Locate every Plasmodium vivax-infected red blood cell.
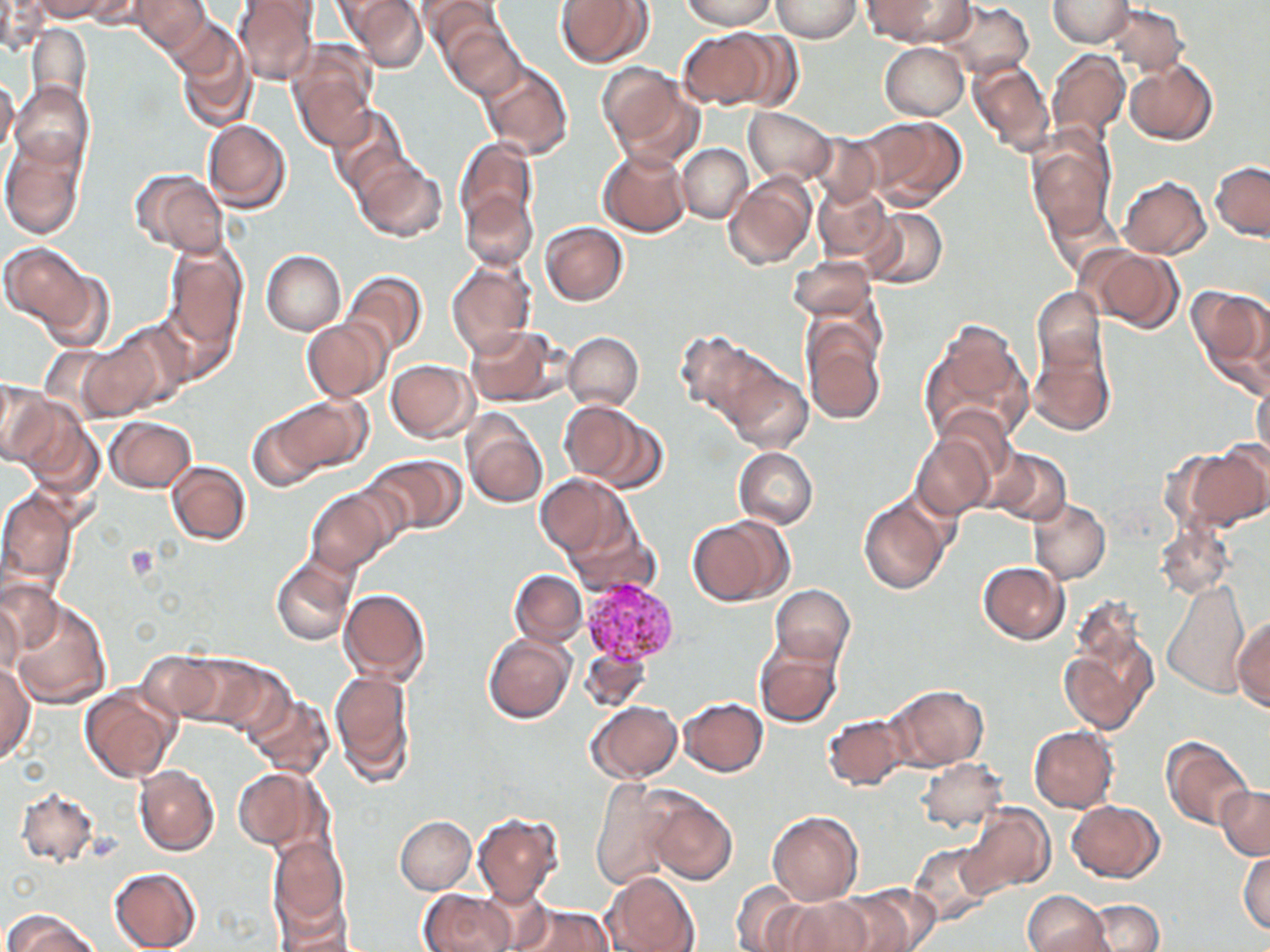

Approximate bounding boxes as (x1,y1)-(x2,y2) corner pairs in pixels.
Plasmodium vivax-infected red blood cells: (581,579)-(678,664).

slide-level diagnosis = Plasmodium vivax
platelet locations = approximate bounding boxes as (x1,y1)-(x2,y2) corner pairs in pixels: (123,545)-(160,581)
stain = May-Grünwald-Giemsa
magnification = 1000x
modality = optical microscopy
field of view = single
uninfected red blood cell locations = approximate bounding boxes as (x1,y1)-(x2,y2) corner pairs in pixels: (32,0)-(110,22), (134,0)-(209,52), (234,0)-(321,84), (346,0)-(426,71), (682,0)-(773,29), (772,0)-(860,42), (865,0)-(966,44), (935,0)-(1033,80), (1048,0)-(1134,49), (417,1)-(503,56), (556,1)-(651,68), (1,2)-(46,54), (1107,3)-(1186,73), (443,22)-(525,99), (26,24)-(93,105), (171,28)-(256,133), (678,28)-(777,109), (718,30)-(804,111), (287,42)-(378,149), (879,43)-(968,120), (1047,51)-(1130,142), (478,60)-(572,159), (967,60)-(1055,153), (1125,60)-(1217,145), (597,63)-(683,149), (0,76)-(18,155), (10,84)-(91,168), (611,85)-(708,172), (328,106)-(410,190), (743,108)-(836,186), (860,115)-(966,210), (202,119)-(291,212), (810,130)-(884,209), (1027,134)-(1117,238), (1,136)-(85,240), (454,137)-(537,231), (678,144)-(753,223), (597,148)-(692,237), (355,158)-(447,242), (1210,162)-(1269,240), (135,170)-(228,257), (724,173)-(816,272), (1119,176)-(1211,259), (813,182)-(892,261), (460,191)-(536,270), (1041,198)-(1123,279), (862,208)-(947,290), (540,222)-(628,306), (164,242)-(246,349), (3,244)-(88,325), (1083,245)-(1183,331), (262,250)-(346,335), (788,255)-(877,321), (447,260)-(534,355), (39,269)-(116,354), (343,271)-(428,356), (1189,286)-(1270,393), (1030,288)-(1106,374), (158,297)-(238,383), (302,318)-(392,402), (921,319)-(1034,448), (802,320)-(886,426), (108,321)-(195,411), (465,325)-(563,407), (563,331)-(643,411), (674,332)-(770,420), (77,337)-(164,420), (1028,340)-(1116,436), (386,359)-(477,441), (721,363)-(812,453), (1252,380)-(1269,465), (0,381)-(59,468), (276,395)-(371,474), (15,402)-(100,494), (935,404)-(1017,484), (579,410)-(667,492), (246,411)-(328,492), (461,412)-(548,509), (106,417)-(196,493), (909,429)-(999,519), (1187,443)-(1270,530), (733,447)-(818,529), (988,448)-(1071,528), (366,455)-(464,534), (167,460)-(250,546), (536,473)-(631,557), (0,487)-(78,594), (306,489)-(393,575), (858,492)-(954,594), (1028,499)-(1110,584), (564,512)-(658,599), (687,516)-(790,605), (1154,523)-(1235,599), (272,559)-(356,647), (978,562)-(1071,643), (510,570)-(586,646), (0,580)-(63,654), (1162,580)-(1251,697), (772,584)-(854,666), (339,588)-(431,684), (7,599)-(112,710), (0,600)-(25,680), (1232,617)-(1269,712), (1059,622)-(1157,734), (484,633)-(575,723), (755,638)-(843,728), (579,642)-(653,714), (138,650)-(226,724), (177,655)-(287,736), (1,662)-(34,764), (329,669)-(415,784), (886,685)-(988,770), (79,687)-(178,784), (245,695)-(334,779), (680,697)-(769,776), (587,700)-(683,783), (822,713)-(911,790), (1028,725)-(1120,812), (1161,738)-(1251,828), (916,758)-(1008,832), (134,765)-(219,856), (232,766)-(326,852), (590,779)-(679,889), (1215,786)-(1269,858), (15,788)-(101,868), (645,793)-(737,885), (1067,801)-(1162,882), (958,804)-(1054,898), (768,811)-(863,906), (472,814)-(563,906), (394,816)-(476,893), (266,835)-(349,938), (910,842)-(1000,927), (1239,850)-(1270,935), (108,868)-(202,952), (604,871)-(699,952), (730,882)-(808,949), (828,887)-(935,952), (420,889)-(518,952), (1022,890)-(1110,952), (270,893)-(359,951), (777,895)-(874,952), (1082,900)-(1164,951), (506,901)-(612,952), (3,910)-(105,952)
image size = 1270×952 pixels
preparation = thin blood film